Classify this cell by malaria status.
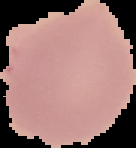

Uninfected.

Cell region segmented out of the field of view; the surrounding area is masked to black. From a thin blood film. Image is 136×148 pixels.